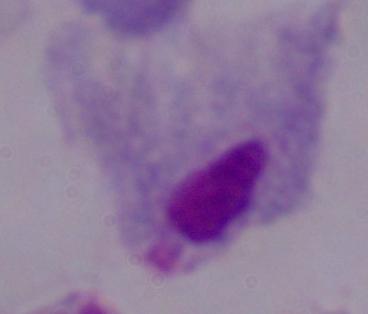
identification = trichomonad
magnification = 1000x
modality = photomicrograph